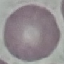
Summary:
  - Malaria status: uninfected
  - Image type: cell patch, automatically extracted from a larger field of view and resized to 64 × 64 pixels
  - Preparation: thin smear
  - Stain: Giemsa
  - Capture: smartphone through the microscope eyepiece